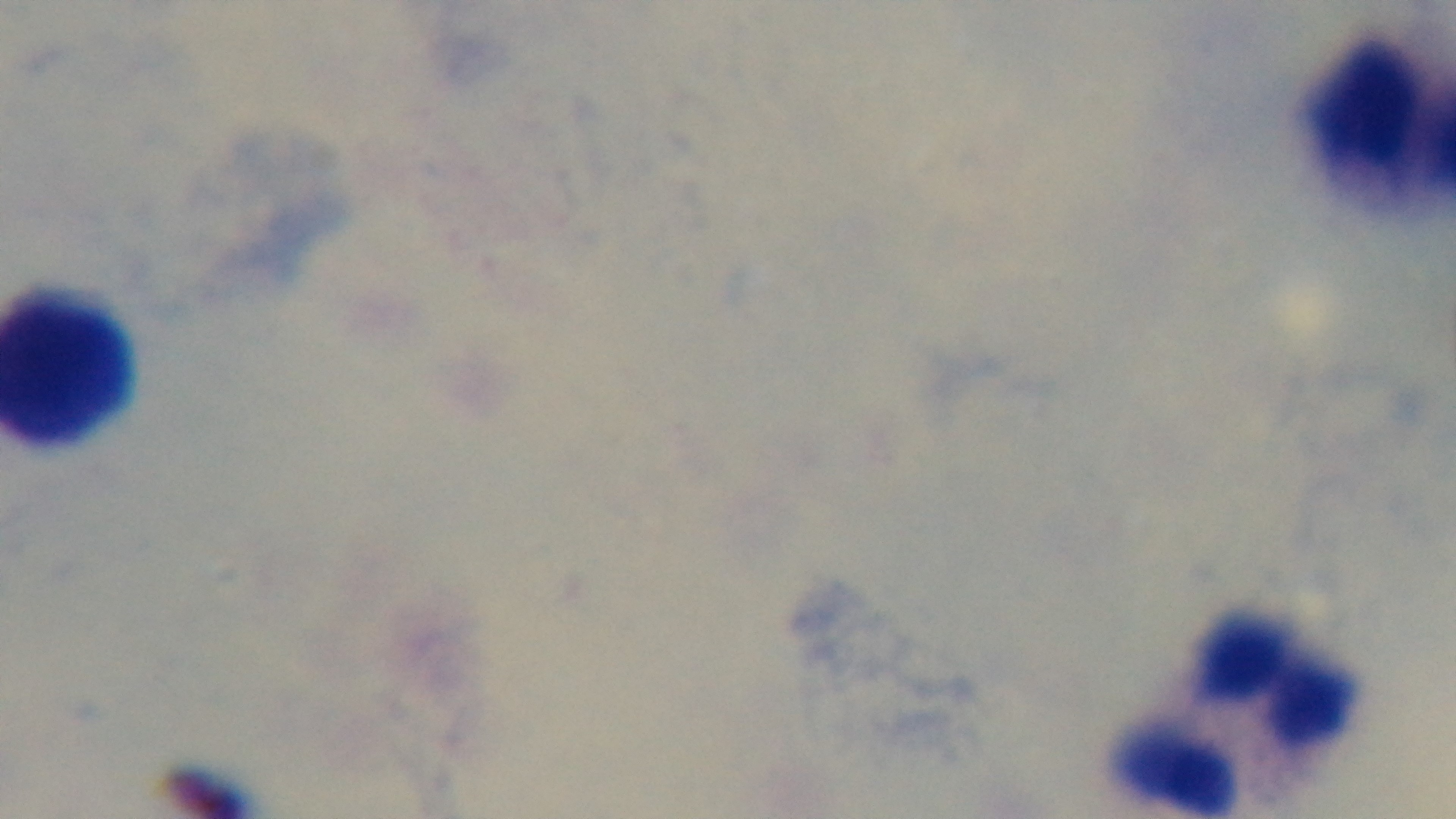
{
  "field_of_view": "single",
  "capture": "mounted 4K digital camera",
  "stain": "Giemsa",
  "preparation": "thick smear",
  "modality": "light microscopy",
  "malaria_status": "uninfected",
  "objective": "100x oil immersion"
}